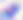 Toxoplasma gondii is seen. Captured at 400x magnification. Photomicrograph.